Outline platelets.
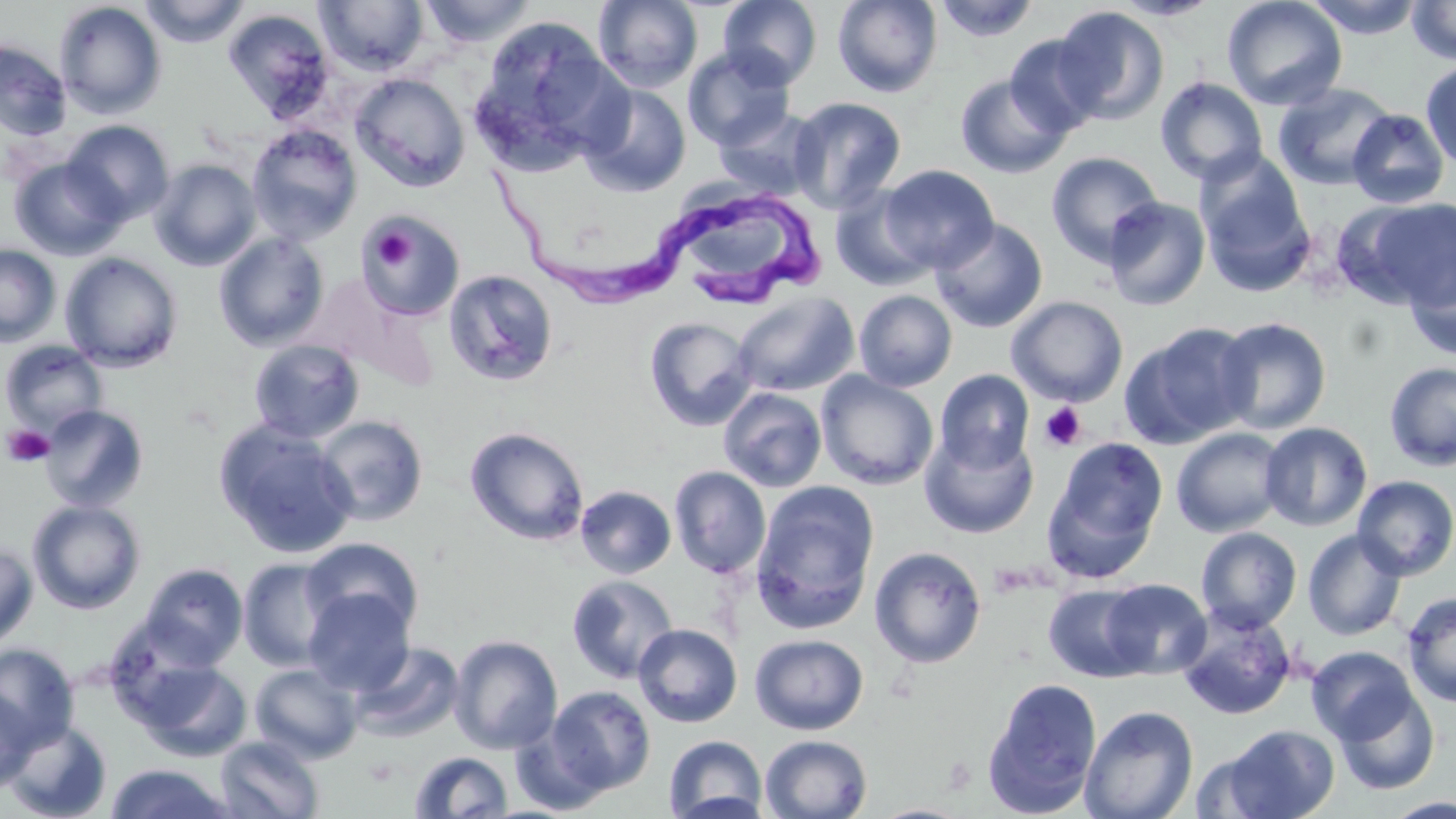
Approximate bounding boxes as (x1,y1)-(x2,y2) corner pairs in pixels.
Platelets: (369,224)-(415,273), (1039,402)-(1087,452), (2,424)-(54,467).

Uninfected red blood cell locations: (139,0)-(251,47), (418,0)-(539,47), (592,0)-(704,92), (718,0)-(822,89), (832,0)-(943,97), (933,0)-(1041,43), (1109,0)-(1223,21), (1222,0)-(1348,111), (1305,0)-(1425,38), (1407,0)-(1456,65), (54,1)-(167,119), (314,1)-(430,76), (1054,6)-(1169,125), (223,8)-(335,124), (469,16)-(626,172), (1005,33)-(1107,137), (1,40)-(72,142), (683,46)-(795,150), (524,56)-(656,192), (1421,60)-(1456,172), (350,73)-(470,192), (954,74)-(1072,179), (1155,77)-(1268,186), (1273,82)-(1396,190), (579,83)-(692,198), (788,96)-(906,213), (713,106)-(823,201), (1347,109)-(1450,209), (61,119)-(174,225), (246,123)-(362,245), (1045,151)-(1163,265), (1195,152)-(1315,293), (9,158)-(126,260), (149,159)-(262,272), (878,164)-(998,272), (682,177)-(787,274), (829,186)-(937,292), (1102,196)-(1211,311), (1349,197)-(1456,309), (357,211)-(464,320), (930,218)-(1048,333), (213,232)-(330,351), (0,244)-(61,347), (1403,250)-(1456,361), (60,252)-(183,372), (442,269)-(559,387), (296,271)-(423,381), (853,289)-(958,392), (731,292)-(859,397), (1006,296)-(1129,406), (642,316)-(758,432), (1213,316)-(1332,435), (1121,321)-(1257,448), (248,339)-(365,444), (1,341)-(107,436), (1384,362)-(1456,472), (934,368)-(1035,472), (816,371)-(938,490), (718,387)-(827,492), (40,404)-(149,512), (313,415)-(429,526), (214,420)-(358,558), (1259,422)-(1372,531), (464,426)-(590,546), (1171,427)-(1287,538), (919,429)-(1038,539), (1044,437)-(1169,580), (669,466)-(771,577), (1352,475)-(1456,580), (751,482)-(879,631), (575,485)-(677,578), (27,499)-(146,614), (1195,527)-(1302,633), (1302,528)-(1407,641), (300,537)-(425,638), (0,544)-(38,652), (869,546)-(987,668), (239,558)-(341,672), (140,563)-(248,668), (566,574)-(679,684), (1100,578)-(1211,679), (1043,583)-(1152,682), (303,588)-(414,696), (1401,591)-(1456,707), (1177,609)-(1296,720), (634,623)-(742,727), (750,633)-(869,735), (449,635)-(563,754), (349,642)-(464,741), (0,643)-(80,750), (1306,645)-(1420,745), (136,659)-(251,761), (249,663)-(363,763), (982,677)-(1103,818), (1333,685)-(1440,796), (546,686)-(656,795), (0,689)-(36,794), (1079,705)-(1199,819), (3,720)-(112,819), (510,724)-(610,815), (1221,724)-(1339,819), (760,734)-(873,819), (215,735)-(324,818), (663,735)-(767,819), (1190,745)-(1281,818), (409,751)-(514,817), (106,763)-(234,819), (1384,798)-(1456,818), (868,803)-(974,819). Trypanosoma brucei locations: (487,159)-(745,305), (689,180)-(835,310). Slide-level diagnosis: Trypanosoma brucei. May-Grünwald-Giemsa stain. Image is 1456×819 pixels. Single field of view. Optical microscopy. 1000x magnification. Thin blood smear.